Report the malaria status of this cell.
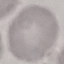
It is uninfected.

preparation: thin blood film
capture: smartphone camera at the microscope eyepiece
stain: Giemsa
image_type: automatically extracted cell patch, resized to 64 × 64 pixels